Identify the cell.
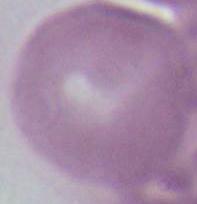

This is an erythrocyte.

Photomicrograph. 1000x magnification.